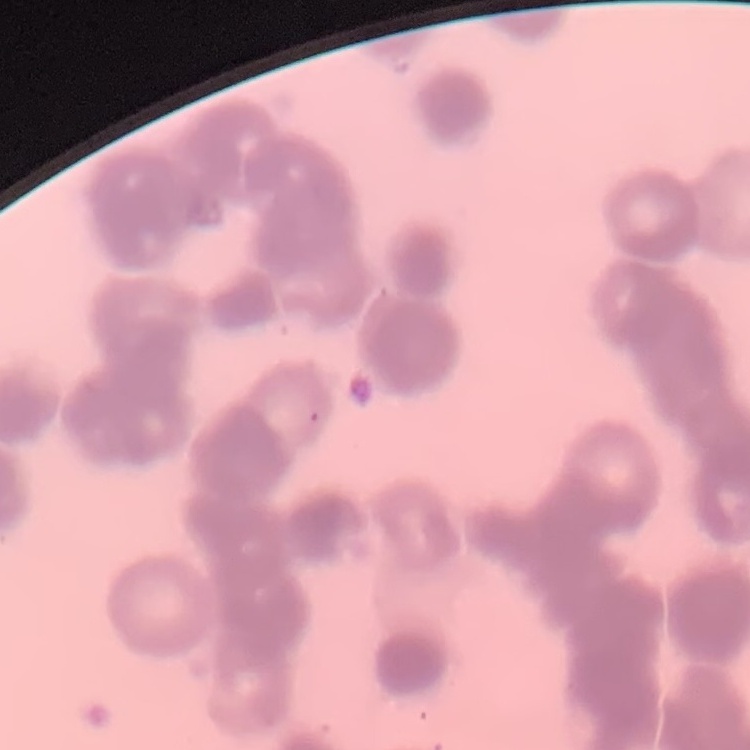 The erythrocytes exhibit rouleaux formation. Field's or Giemsa stain. Square crop of a larger photomicrograph. Thin blood film.